Report the malaria status of this cell.
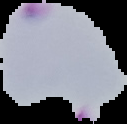
It is parasitized.

Summary:
  - Image size: 127×124 pixels
  - Preparation: thin blood film
  - Image type: cell region segmented out of the field of view; surrounding area masked to black